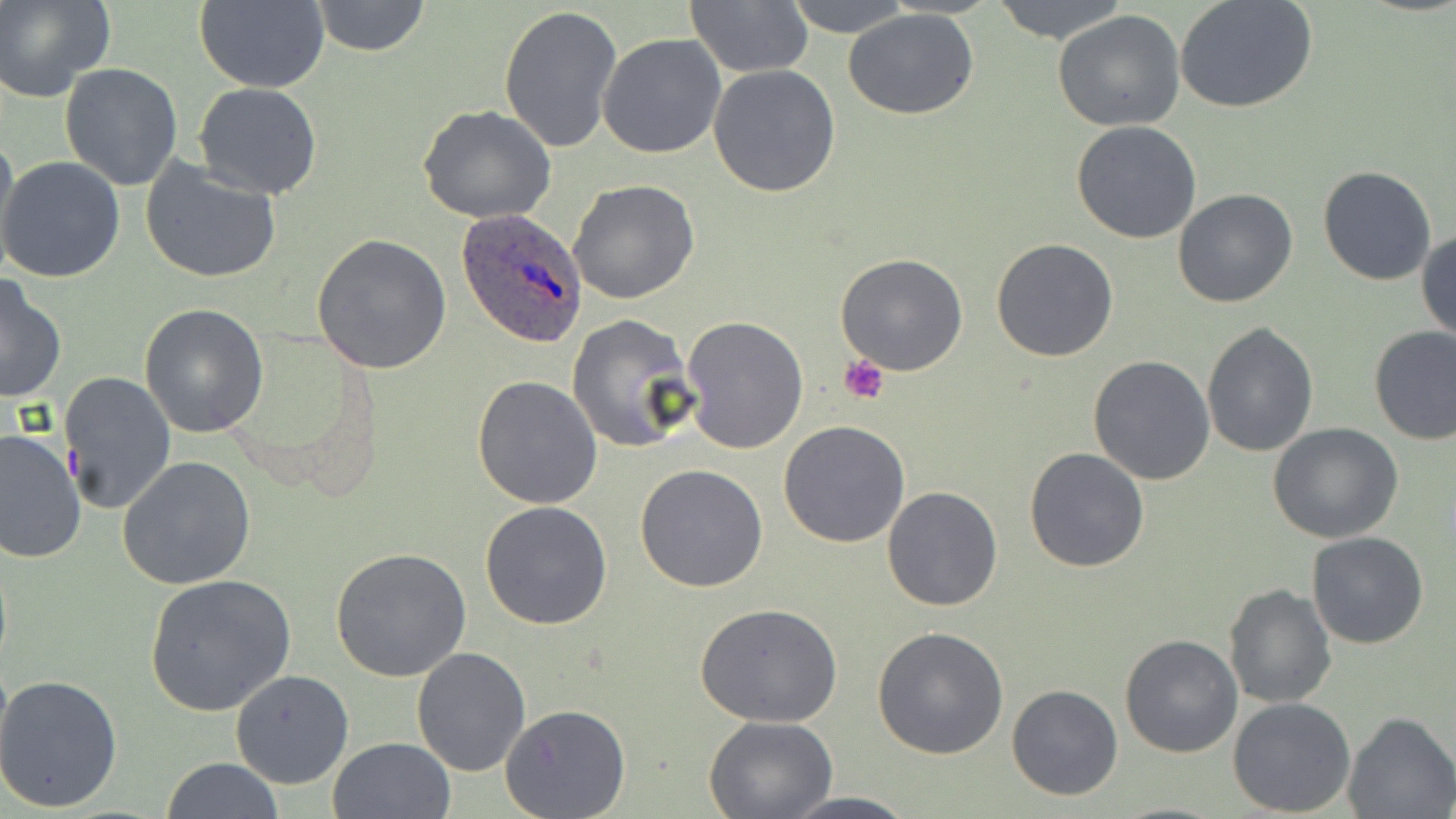
slide-level diagnosis = Plasmodium ovale
stain = May-Grünwald-Giemsa
platelet locations = approximate bounding boxes as (x1,y1)-(x2,y2) corner pairs in pixels: (839,354)-(890,404)
preparation = thin blood smear
magnification = 1000x
Plasmodium ovale-infected red blood cell locations = approximate bounding boxes as (x1,y1)-(x2,y2) corner pairs in pixels: (456,208)-(587,348)
image size = 1456×819 pixels
field of view = one of a larger specimen
modality = light microscopy
uninfected red blood cell locations = approximate bounding boxes as (x1,y1)-(x2,y2) corner pairs in pixels: (1,0)-(113,104), (311,0)-(432,57), (782,0)-(916,37), (990,0)-(1131,45), (1174,0)-(1317,114), (193,1)-(329,92), (683,2)-(813,78), (499,5)-(622,154), (842,8)-(979,121), (1053,10)-(1185,132), (598,34)-(726,157), (60,63)-(183,190), (708,66)-(841,197), (193,82)-(323,199), (418,104)-(556,224), (1072,121)-(1201,243), (0,128)-(18,267), (1,157)-(126,283), (139,157)-(283,283), (1317,164)-(1437,285), (569,179)-(698,303), (1172,188)-(1298,308), (1416,228)-(1456,343), (312,233)-(452,376), (991,236)-(1120,362), (835,252)-(969,375), (0,274)-(68,404), (138,303)-(269,439), (567,313)-(697,452), (680,314)-(809,453), (1200,322)-(1319,458), (1368,325)-(1455,445), (1088,355)-(1217,485), (58,370)-(177,514), (472,374)-(603,508), (778,420)-(911,548), (1267,422)-(1403,544), (1,430)-(86,564), (1023,446)-(1149,573), (117,456)-(257,591), (635,463)-(769,592), (881,485)-(1002,612), (480,500)-(614,630), (1305,531)-(1429,649), (331,548)-(473,684), (144,574)-(297,715), (1224,582)-(1336,711), (695,602)-(845,728), (872,627)-(1009,759), (1119,634)-(1244,758), (410,646)-(530,776), (230,669)-(353,789), (0,673)-(123,814), (1007,685)-(1125,801), (1228,697)-(1356,817), (501,705)-(630,818), (1343,712)-(1454,819), (705,714)-(836,817), (327,736)-(455,819), (161,758)-(283,818), (773,791)-(922,819)